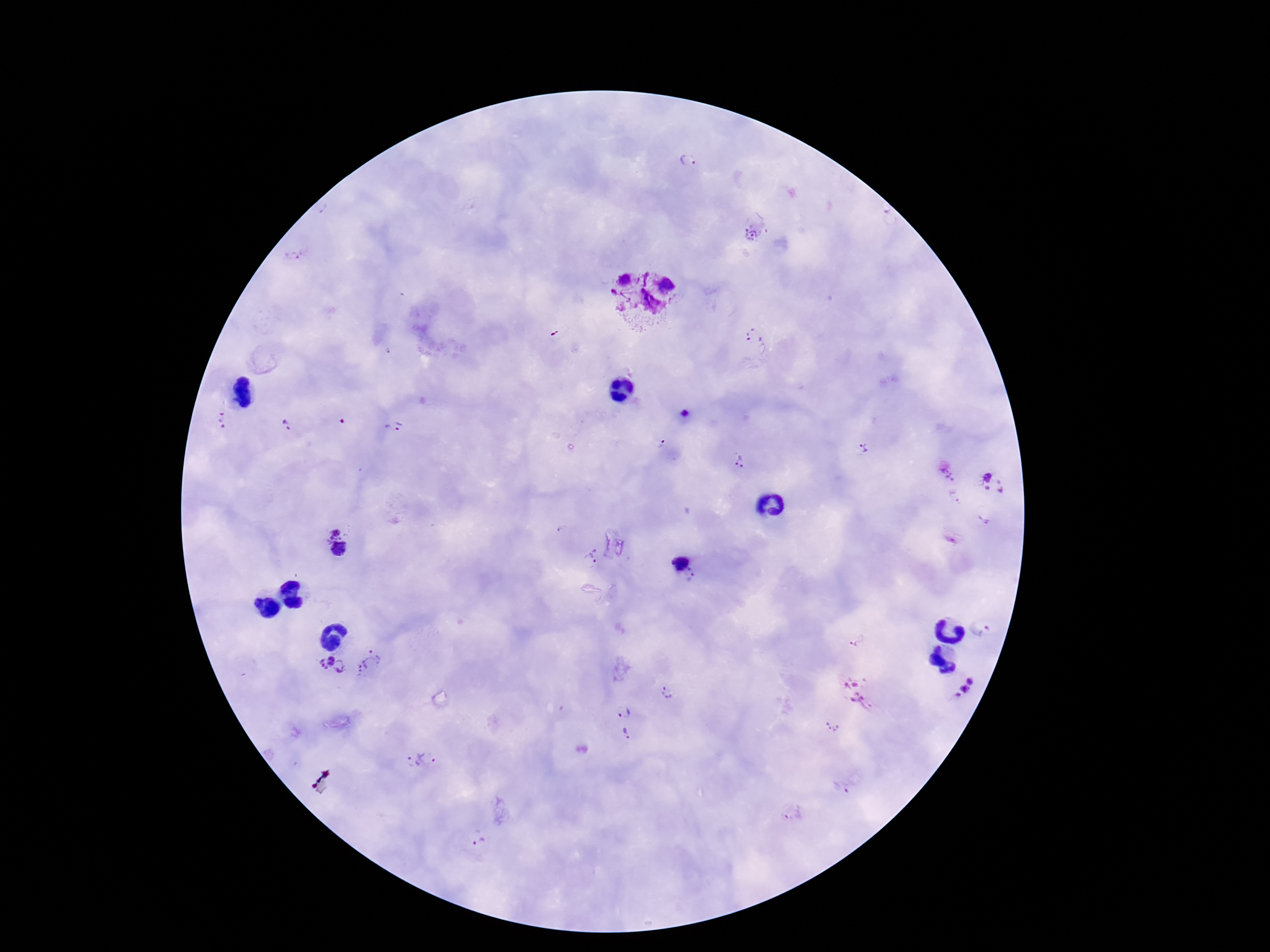

Approximate centers as (x, y) in pixels.
Summary:
  - Plasmodium parasite locations: (687, 160), (754, 227), (645, 299), (755, 336), (218, 422), (288, 426), (397, 426), (659, 445), (861, 449), (742, 461), (950, 473), (993, 483), (953, 496), (984, 519), (336, 544), (591, 556), (677, 558), (694, 578), (987, 628), (856, 639), (370, 663), (332, 667), (961, 683), (855, 691), (667, 693), (623, 711), (832, 728), (626, 734), (431, 757), (411, 759), (840, 787), (792, 814), (479, 843)
  - Field of view: single
  - Magnification: 100x
  - Preparation: thick peripheral-blood smear
  - Image size: 1270×952 pixels
  - Patient malaria status: infected
  - Capture: smartphone camera through the microscope eyepiece
  - Stain: Giemsa